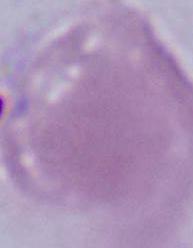
A red blood cell is shown. Photomicrograph. Captured at 1000x magnification.